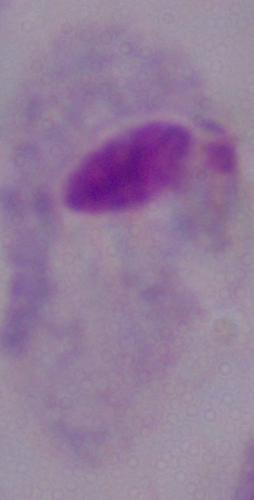

Summary:
  - Identification: trichomonad
  - Magnification: 1000x
  - Modality: photomicrograph